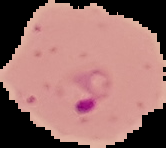

Cell region segmented out of the field of view; the surrounding area is masked to black. Image is 166×148 pixels. Malaria status: parasitized. From a thin blood smear.